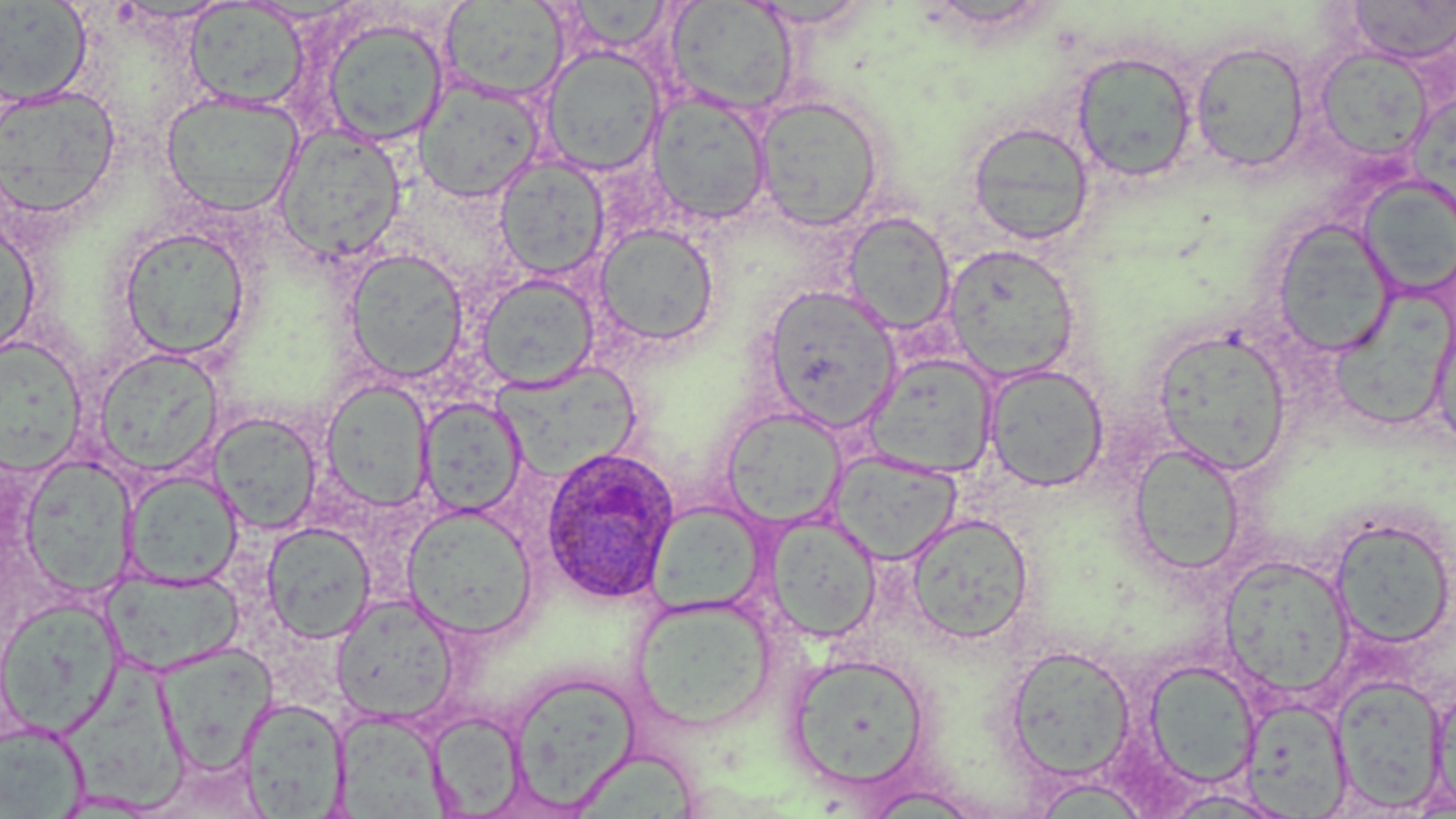

Approximate bounding boxes as named x1/y1/x2/y2 corners in pixels. Plasmodium ovale-infected red blood cell locations: (x1=539, y1=445, x2=680, y2=605). Uninfected red blood cell locations: (x1=1346, y1=0, x2=1456, y2=65), (x1=0, y1=1, x2=93, y2=106), (x1=439, y1=1, x2=569, y2=102), (x1=564, y1=1, x2=674, y2=53), (x1=665, y1=1, x2=799, y2=117), (x1=744, y1=1, x2=876, y2=30), (x1=184, y1=2, x2=310, y2=111), (x1=320, y1=16, x2=450, y2=147), (x1=1190, y1=39, x2=1311, y2=174), (x1=1314, y1=46, x2=1432, y2=164), (x1=540, y1=47, x2=666, y2=176), (x1=1071, y1=50, x2=1199, y2=183), (x1=414, y1=78, x2=545, y2=203), (x1=0, y1=85, x2=122, y2=220), (x1=160, y1=91, x2=303, y2=217), (x1=646, y1=91, x2=773, y2=226), (x1=754, y1=95, x2=887, y2=232), (x1=967, y1=120, x2=1095, y2=246), (x1=274, y1=125, x2=407, y2=263), (x1=495, y1=155, x2=610, y2=279), (x1=1356, y1=176, x2=1456, y2=298), (x1=841, y1=211, x2=956, y2=336), (x1=0, y1=219, x2=41, y2=362), (x1=1270, y1=219, x2=1398, y2=357), (x1=593, y1=223, x2=720, y2=348), (x1=116, y1=225, x2=252, y2=361), (x1=943, y1=243, x2=1081, y2=382), (x1=343, y1=248, x2=469, y2=383), (x1=475, y1=272, x2=600, y2=391), (x1=762, y1=286, x2=901, y2=429), (x1=1327, y1=293, x2=1448, y2=436), (x1=1430, y1=312, x2=1456, y2=454), (x1=1152, y1=327, x2=1293, y2=475), (x1=0, y1=336, x2=90, y2=474), (x1=93, y1=347, x2=224, y2=478), (x1=864, y1=353, x2=999, y2=478), (x1=488, y1=359, x2=641, y2=482), (x1=984, y1=364, x2=1109, y2=492), (x1=320, y1=378, x2=435, y2=511), (x1=417, y1=397, x2=526, y2=518), (x1=721, y1=408, x2=847, y2=529), (x1=209, y1=413, x2=323, y2=535), (x1=1127, y1=442, x2=1247, y2=576), (x1=830, y1=450, x2=962, y2=564), (x1=20, y1=454, x2=136, y2=599), (x1=122, y1=469, x2=244, y2=588), (x1=646, y1=502, x2=768, y2=616), (x1=402, y1=506, x2=537, y2=641), (x1=763, y1=512, x2=882, y2=643), (x1=904, y1=512, x2=1034, y2=644), (x1=1329, y1=517, x2=1455, y2=650), (x1=261, y1=521, x2=377, y2=644), (x1=1219, y1=554, x2=1357, y2=699), (x1=102, y1=568, x2=245, y2=676), (x1=630, y1=594, x2=779, y2=732), (x1=332, y1=595, x2=459, y2=723), (x1=0, y1=596, x2=124, y2=737), (x1=154, y1=642, x2=277, y2=773), (x1=1003, y1=644, x2=1137, y2=782), (x1=786, y1=651, x2=932, y2=790), (x1=66, y1=658, x2=192, y2=816), (x1=1143, y1=659, x2=1261, y2=790), (x1=506, y1=669, x2=641, y2=812), (x1=1333, y1=672, x2=1450, y2=814), (x1=1428, y1=676, x2=1455, y2=815), (x1=1240, y1=696, x2=1353, y2=817), (x1=239, y1=698, x2=348, y2=817), (x1=335, y1=711, x2=460, y2=819), (x1=425, y1=711, x2=528, y2=816), (x1=0, y1=719, x2=90, y2=817), (x1=1028, y1=776, x2=1157, y2=818), (x1=857, y1=784, x2=989, y2=817), (x1=1155, y1=788, x2=1296, y2=818). Slide-level diagnosis: Plasmodium ovale. Thin blood smear. Captured at 1000x magnification. May-Grünwald-Giemsa stain. Image is 1456×819 pixels. One field of a larger specimen. Optical microscopy.